Classify this cell by malaria status.
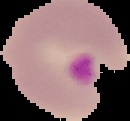

Parasitized.

Image is 130×121 pixels. Segmented cell region on a black background. From a thin blood smear.